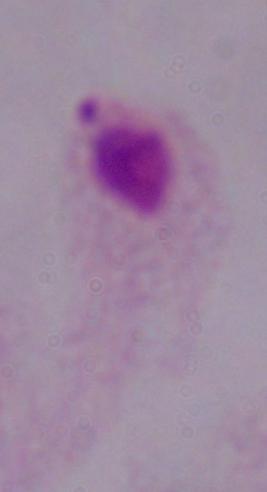
Summary:
  - Magnification: 1000x
  - Modality: photomicrograph
  - Identification: trichomonad